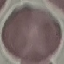

malaria_status: uninfected
capture: smartphone through the microscope eyepiece
stain: Giemsa
image_type: automatically extracted cell patch, resized to 64 × 64 pixels
preparation: thin blood smear